Identify the preparation type.
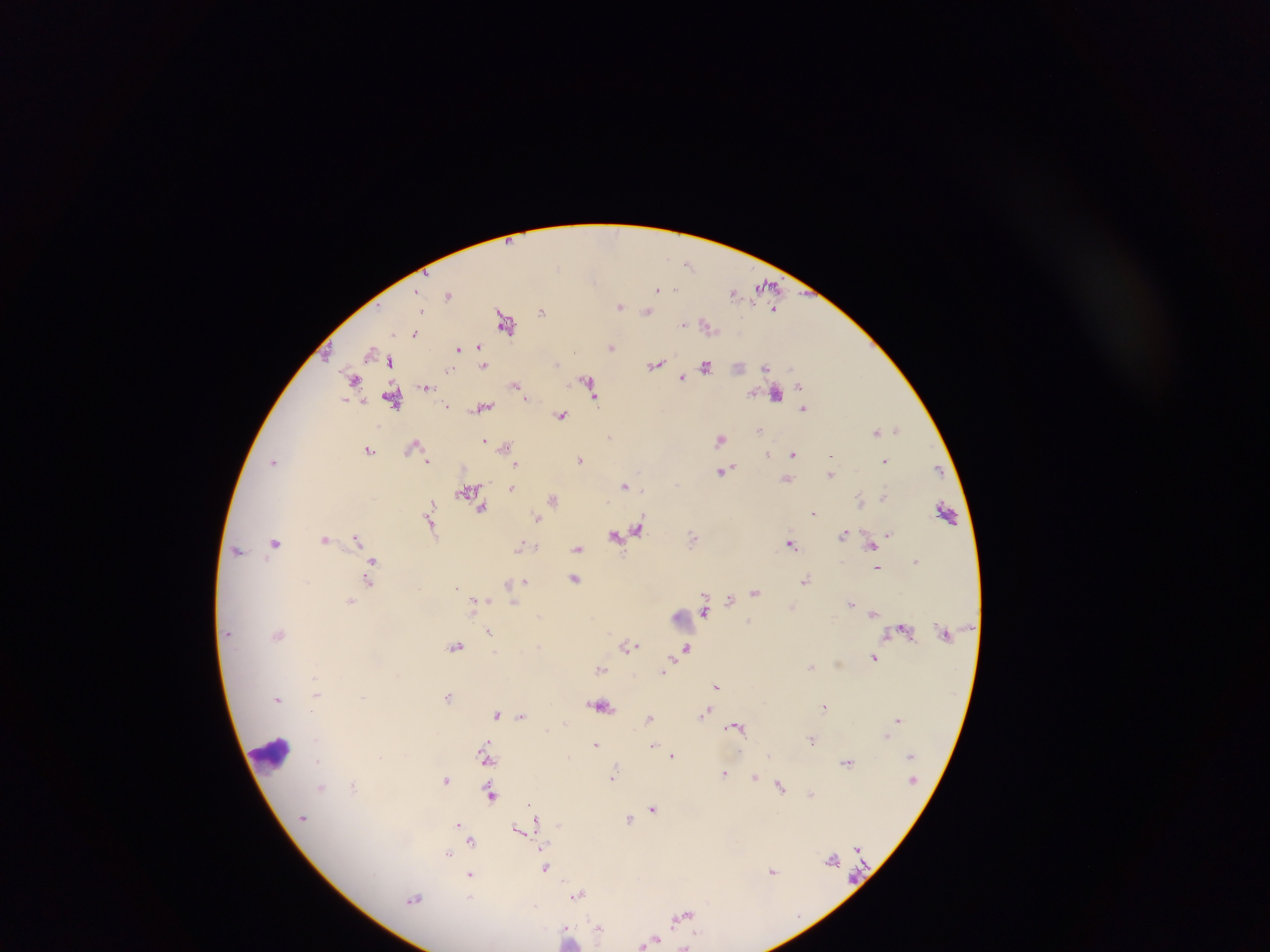

This is a thick smear.

malaria_parasite_locations: 'approximate centers as (x, y) in pixels: (689, 263), (765, 287), (676, 290), (657, 291), (735, 292), (449, 294), (620, 306), (543, 311), (423, 312), (647, 312), (506, 323), (683, 324), (416, 332), (479, 346), (612, 347), (457, 348), (370, 353), (388, 359), (655, 365), (706, 366), (484, 367), (766, 369), (352, 377), (683, 377), (799, 383), (589, 384), (515, 385), (428, 386), (753, 394), (775, 395), (528, 398), (594, 398), (392, 399), (346, 400), (447, 406), (484, 406), (805, 407), (561, 416), (897, 429), (760, 430), (877, 431), (485, 439), (721, 439), (415, 446), (505, 446), (369, 450), (793, 453), (428, 460), (581, 460), (885, 461), (734, 464), (517, 466), (731, 467), (721, 472), (832, 473), (677, 484), (624, 485), (512, 488), (466, 492), (883, 496), (861, 498), (553, 499), (432, 504), (483, 510), (943, 511), (815, 512), (538, 517), (430, 527), (639, 529), (626, 532), (846, 533), (888, 534), (614, 535), (356, 536), (694, 536), (324, 540), (275, 544), (789, 544), (872, 546), (520, 548), (578, 549), (239, 550), (374, 560), (915, 561), (877, 568), (576, 578), (368, 580), (806, 580), (527, 581), (508, 583), (756, 592), (730, 599), (474, 600), (485, 600), (351, 601), (513, 603), (850, 603), (704, 612), (871, 615), (749, 621), (489, 630), (278, 633), (457, 646), (628, 646), (687, 646), (495, 653), (874, 657), (839, 663), (669, 664), (812, 666), (601, 669), (664, 670), (315, 676), (718, 686), (318, 695), (449, 697), (278, 700), (600, 705), (824, 707), (709, 709), (706, 713), (497, 715), (521, 717), (648, 718), (703, 718), (896, 718), (732, 726), (741, 726), (885, 736), (813, 738), (597, 743), (485, 744), (652, 747), (674, 755), (379, 756), (767, 756), (316, 760), (486, 762), (846, 763), (615, 770), (726, 773), (756, 776), (615, 777), (448, 780), (353, 784), (321, 786), (781, 786), (812, 794), (492, 797), (528, 802), (653, 806), (629, 818), (536, 820), (456, 823), (558, 824), (535, 825), (516, 828), (471, 841), (448, 855), (831, 858), (545, 867), (772, 871), (471, 877), (579, 894), (469, 896), (415, 898), (686, 914), (675, 917), (596, 922), (567, 924), (599, 927), (651, 939)'
field_of_view: single
image_size: 1270×952 pixels
country: Ghana
leukocyte_locations: 'approximate centers as (x, y) in pixels: (275, 758)'
capture: mobile-phone photograph through a microscope